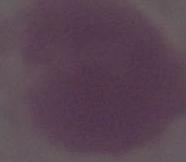
Summary:
  - Identification: red blood cell
  - Modality: photomicrograph
  - Magnification: 1000x